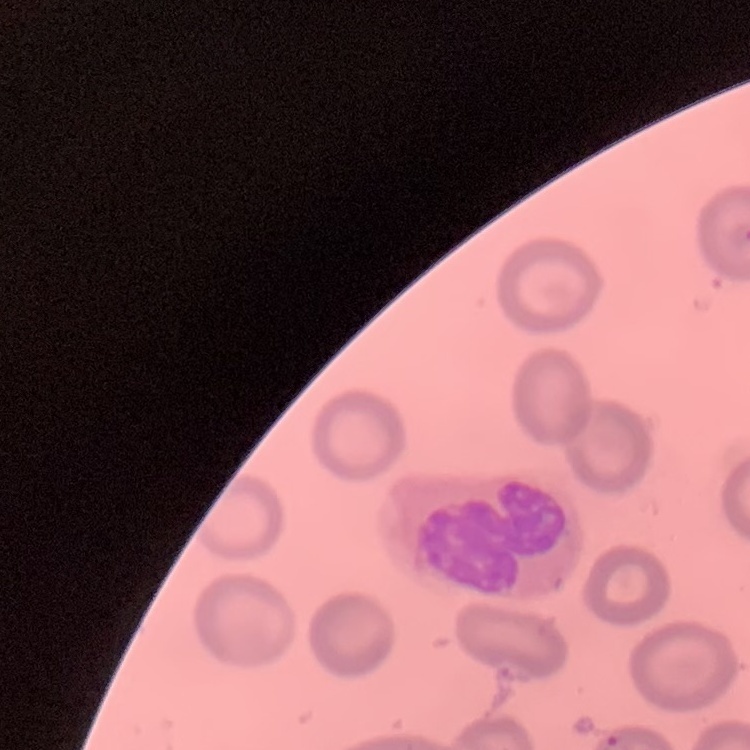
{
  "erythrocyte_morphology": "no rouleaux formation",
  "image_type": "square crop of a larger photomicrograph",
  "stain": "Field's or Giemsa",
  "preparation": "thin blood film"
}